Assess this cell for malaria.
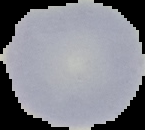
Uninfected.

From a thin blood film. Cell region segmented out of the field of view; the surrounding area is masked to black. Image is 145×130 pixels.